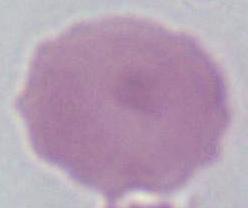

modality = micrograph
magnification = 1000x
identification = red blood cell